Assess the morphology of the red blood cells.
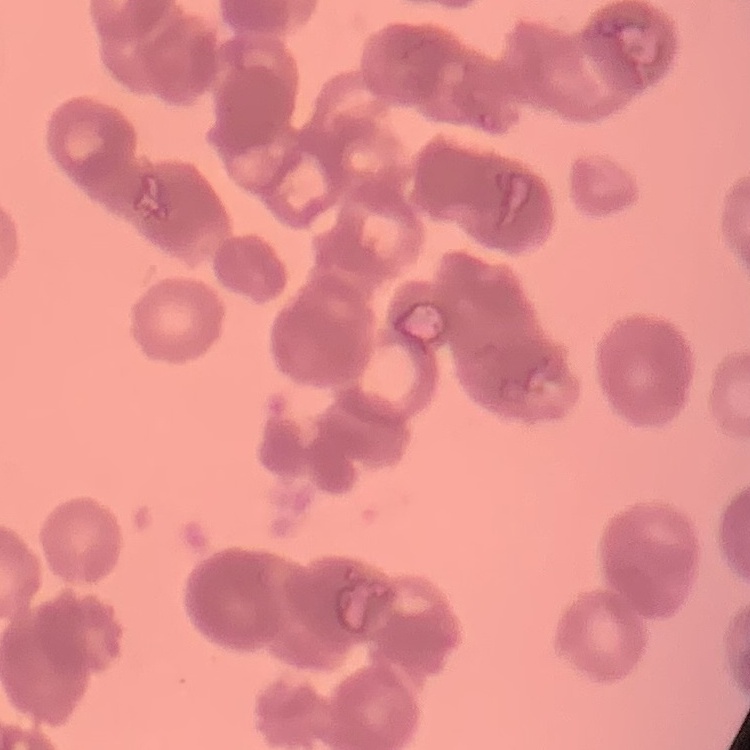

Rouleaux formation.

preparation = thin blood film
image type = one tile cut from a larger photomicrograph
stain = Field's or Giemsa